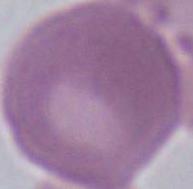
identification: erythrocyte
modality: micrograph
magnification: 1000x